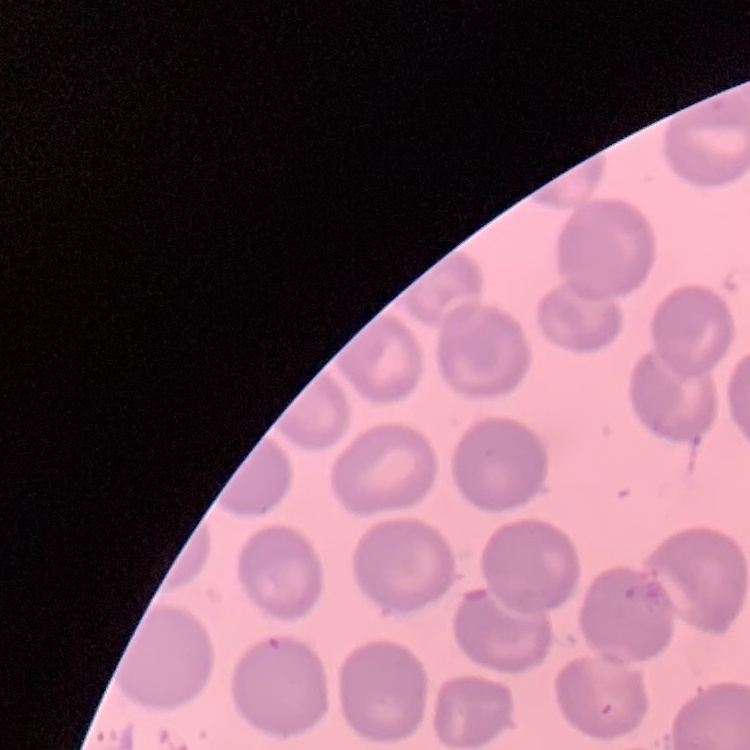
The red blood cells exhibit no rouleaux formation. One tile cut from a larger photomicrograph. Stained with either Field's or Giemsa. Thin peripheral smear.